State which parasite is depicted.
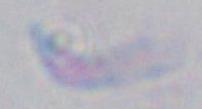

This is Toxoplasma gondii.

modality = micrograph
magnification = 1000x